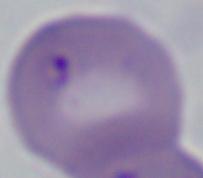
Summary:
  - Identification: Babesia
  - Magnification: 1000x
  - Modality: photomicrograph